State the preparation type.
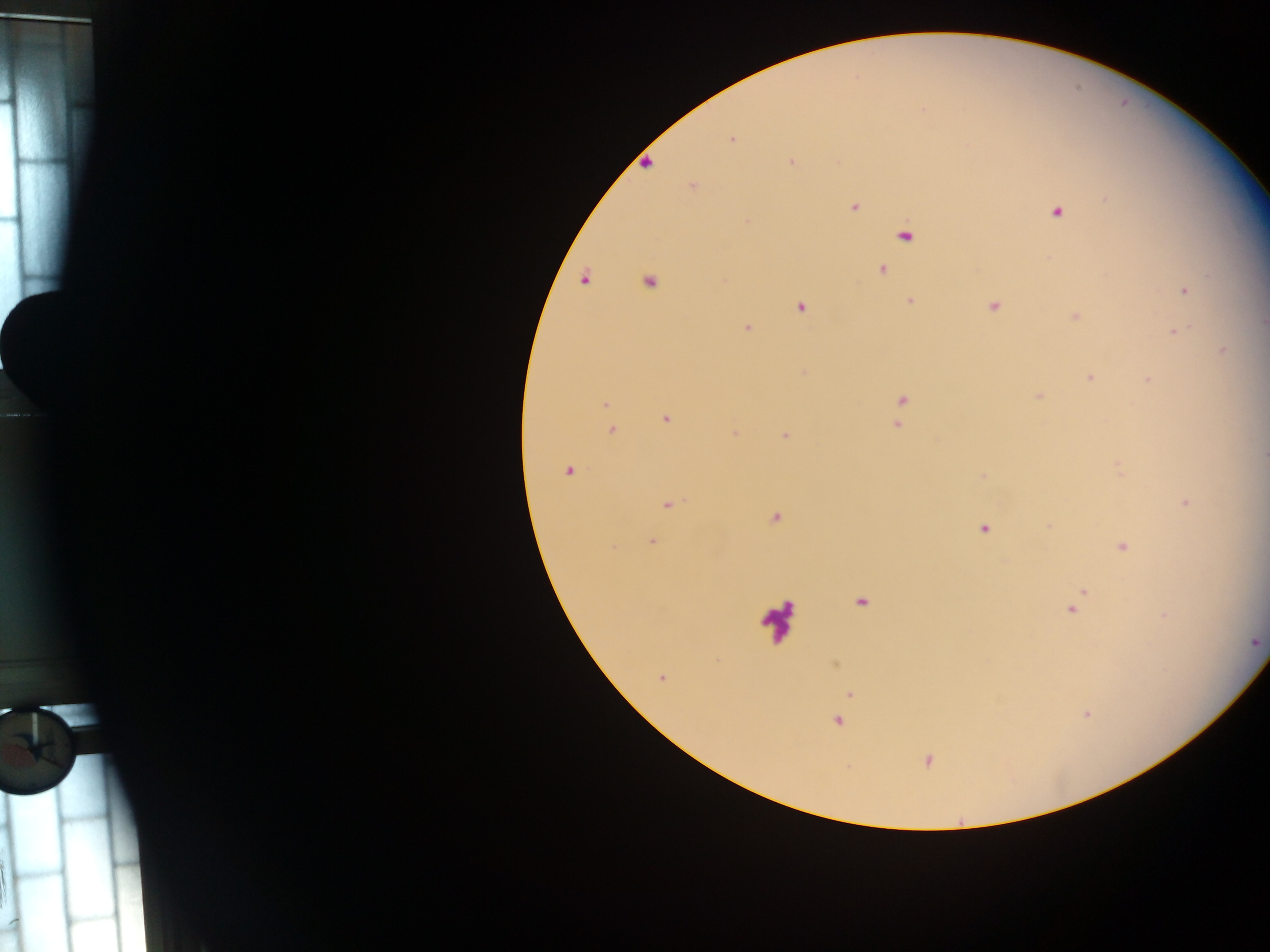

Thick blood smear.

image size = 1270×952 pixels
malaria parasite locations = approximate centers as (x, y) in pixels: (731, 140), (790, 161), (692, 186), (854, 207), (1057, 212), (905, 236), (882, 270), (584, 280), (649, 282), (1185, 291), (910, 301), (993, 306), (801, 308), (1076, 316), (1263, 324), (747, 327), (1175, 332), (1224, 350), (1090, 378), (1147, 380), (901, 400), (605, 404), (665, 419), (897, 425), (612, 430), (735, 434), (785, 436), (1264, 455), (569, 471), (1185, 502), (669, 505), (774, 519), (1049, 526), (985, 529), (653, 541), (1123, 547), (1083, 592), (860, 603), (1072, 610), (1256, 643), (661, 678), (850, 694), (837, 721), (928, 761)
country = Ghana
capture = mobile-phone photograph through a microscope
field of view = single
leukocyte locations = approximate centers as (x, y) in pixels: (777, 619)